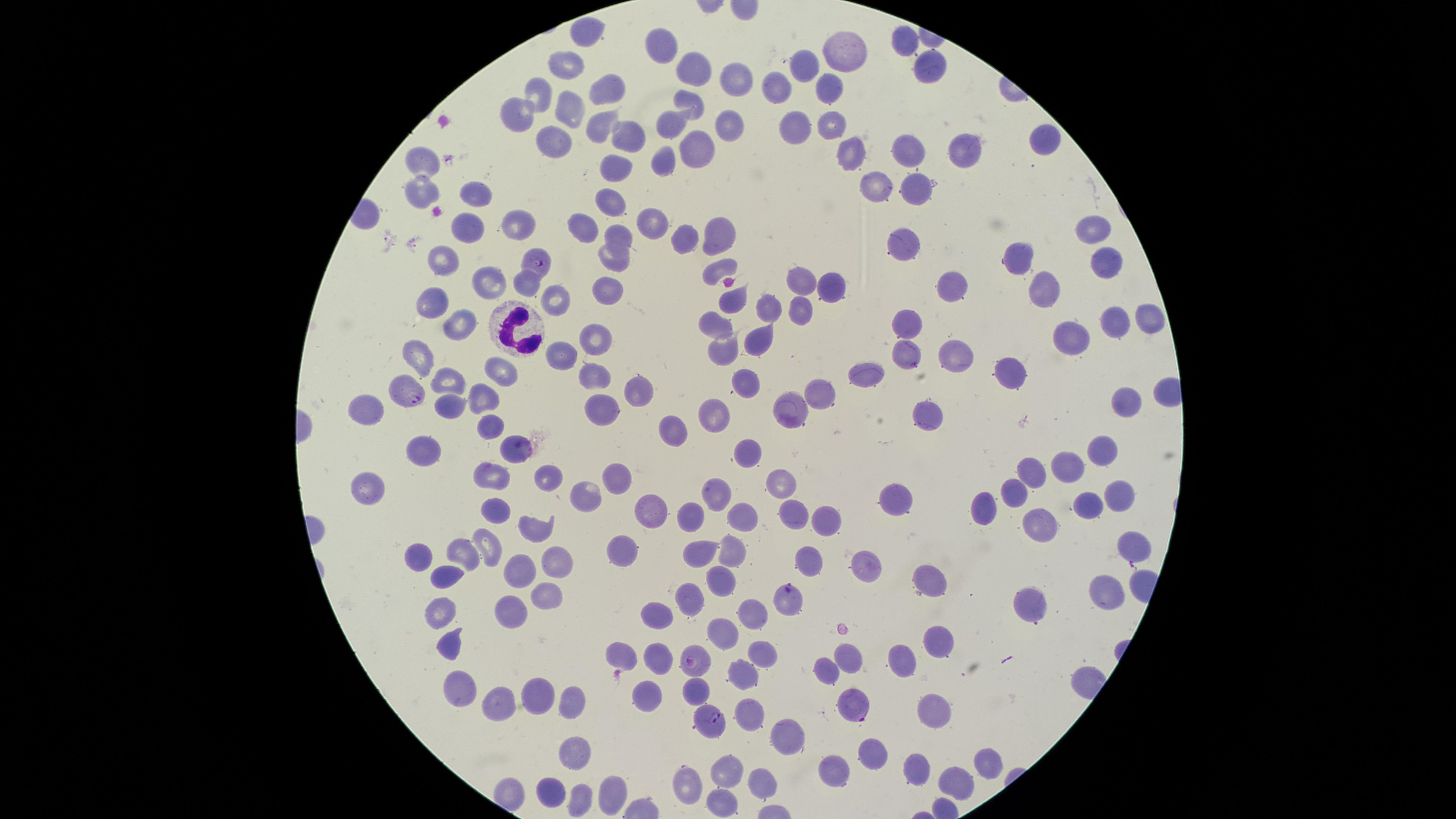
Approximate marker points, in pixels from the top-left corner.
Summary:
  - White blood cells: (x=514, y=328)
  - Parasitized red blood cells: (x=538, y=263), (x=406, y=393), (x=789, y=598), (x=693, y=662), (x=859, y=706), (x=712, y=722)
  - Uninfected red blood cells: (x=581, y=33), (x=660, y=47), (x=900, y=47), (x=840, y=52), (x=564, y=63), (x=926, y=65), (x=803, y=67), (x=694, y=69), (x=734, y=80), (x=603, y=87), (x=777, y=88), (x=830, y=90), (x=533, y=91), (x=689, y=104), (x=566, y=108), (x=514, y=113), (x=720, y=120), (x=595, y=122), (x=798, y=123), (x=834, y=123), (x=671, y=125), (x=617, y=130), (x=1044, y=138), (x=552, y=141), (x=953, y=152), (x=895, y=153), (x=692, y=154), (x=418, y=159), (x=855, y=159), (x=666, y=169), (x=617, y=171), (x=872, y=185), (x=917, y=188), (x=416, y=190), (x=474, y=192), (x=610, y=202), (x=647, y=223), (x=464, y=224), (x=512, y=224), (x=580, y=226), (x=1089, y=229), (x=617, y=237), (x=681, y=239), (x=715, y=240), (x=898, y=241), (x=1012, y=255), (x=613, y=258), (x=441, y=261), (x=1100, y=262), (x=717, y=265), (x=522, y=279), (x=485, y=281), (x=794, y=282), (x=836, y=284), (x=951, y=285), (x=1044, y=289), (x=557, y=299), (x=608, y=299), (x=733, y=306), (x=431, y=307), (x=794, y=309), (x=761, y=310), (x=908, y=321), (x=1149, y=322), (x=1114, y=323), (x=716, y=324), (x=460, y=329), (x=596, y=330), (x=756, y=338), (x=1063, y=339), (x=727, y=351), (x=954, y=353), (x=568, y=354), (x=903, y=354), (x=418, y=358), (x=1008, y=371), (x=494, y=373), (x=863, y=373), (x=588, y=375), (x=445, y=377), (x=745, y=384), (x=638, y=386), (x=826, y=389), (x=479, y=394), (x=1124, y=401), (x=602, y=403), (x=792, y=404), (x=364, y=405), (x=439, y=406), (x=919, y=410), (x=716, y=416), (x=490, y=427), (x=668, y=430), (x=1102, y=446), (x=512, y=448), (x=748, y=451), (x=414, y=454), (x=1071, y=466), (x=1030, y=473), (x=542, y=475), (x=492, y=476), (x=617, y=478), (x=783, y=479), (x=371, y=488), (x=1114, y=490), (x=585, y=493), (x=716, y=493), (x=1016, y=493), (x=894, y=496), (x=981, y=503), (x=495, y=504), (x=1086, y=504), (x=651, y=510), (x=788, y=511), (x=740, y=515), (x=527, y=518), (x=692, y=518), (x=818, y=520), (x=1033, y=524), (x=491, y=543), (x=619, y=546), (x=1131, y=548), (x=700, y=549), (x=729, y=549), (x=412, y=550), (x=460, y=554), (x=806, y=560), (x=551, y=561), (x=862, y=566), (x=511, y=569), (x=438, y=574), (x=928, y=578), (x=720, y=582), (x=547, y=591), (x=1105, y=591), (x=685, y=596), (x=1025, y=607), (x=749, y=609), (x=655, y=612), (x=435, y=613), (x=502, y=619), (x=720, y=630), (x=452, y=639), (x=932, y=642), (x=614, y=651), (x=654, y=656), (x=845, y=656), (x=755, y=657), (x=902, y=661), (x=824, y=667), (x=739, y=675), (x=459, y=684), (x=698, y=685), (x=536, y=695), (x=638, y=696), (x=571, y=698), (x=496, y=703), (x=935, y=705), (x=750, y=708), (x=781, y=740), (x=865, y=751), (x=576, y=752), (x=724, y=766), (x=980, y=768), (x=828, y=769), (x=913, y=769), (x=759, y=775), (x=691, y=779), (x=949, y=782), (x=548, y=785), (x=608, y=791), (x=575, y=797), (x=712, y=800)
  - Visible region: circular
  - Presence: malaria parasites seen
  - Capture: smartphone photograph through the microscope eyepiece
  - Field of view: single
  - Stain: Giemsa
  - Image size: 1456×819 pixels
  - Preparation: thin blood smear
  - Species: Plasmodium falciparum